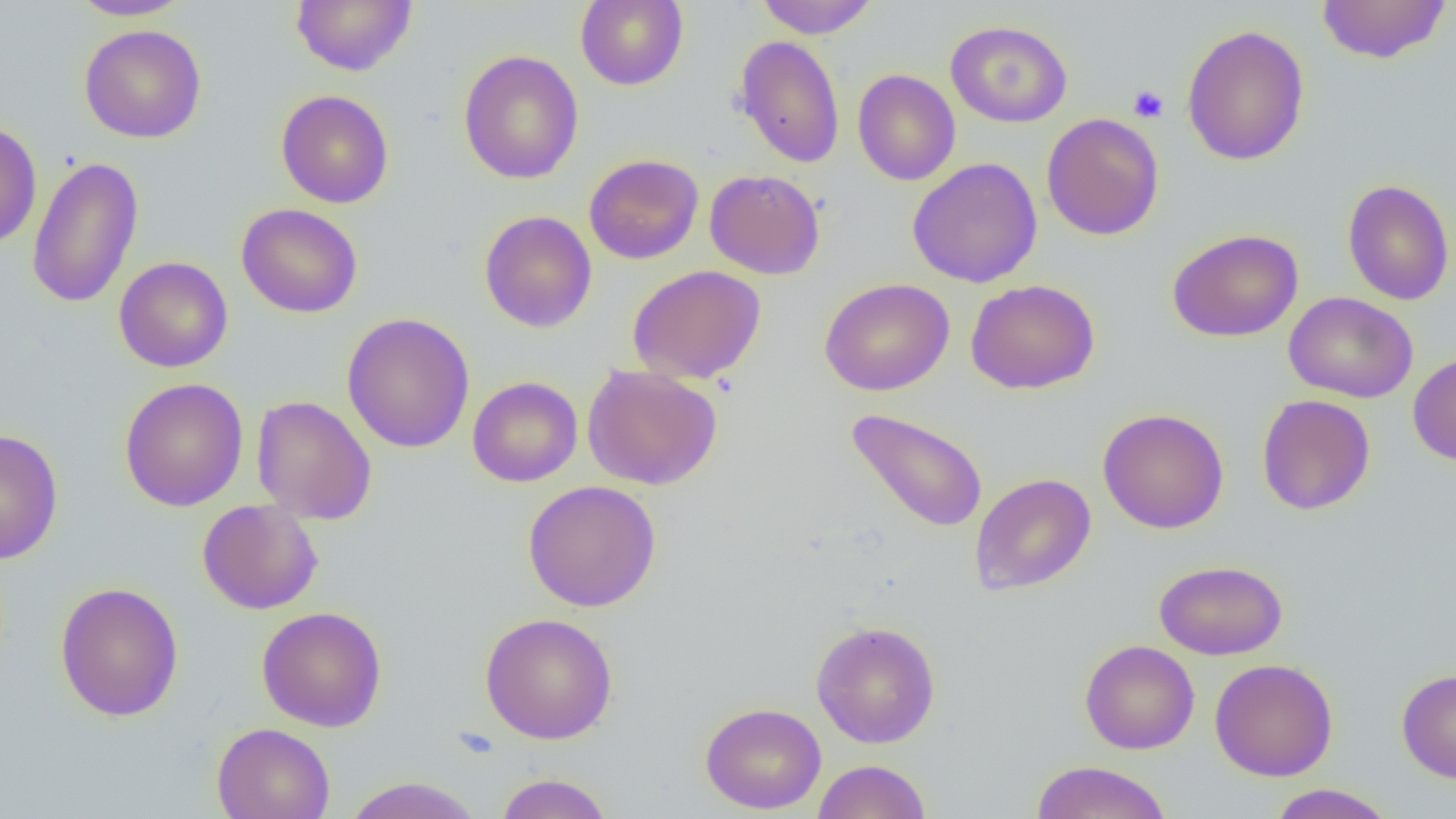

Approximate bounding boxes as named x1/y1/x2/y2 corners in pixels. Uninfected red blood cell locations: (x1=69, y1=0, x2=195, y2=21), (x1=291, y1=0, x2=417, y2=76), (x1=575, y1=0, x2=689, y2=91), (x1=755, y1=0, x2=879, y2=39), (x1=1316, y1=0, x2=1453, y2=64), (x1=945, y1=20, x2=1073, y2=127), (x1=1181, y1=23, x2=1310, y2=166), (x1=79, y1=24, x2=207, y2=143), (x1=734, y1=35, x2=846, y2=169), (x1=458, y1=49, x2=584, y2=184), (x1=852, y1=69, x2=960, y2=186), (x1=276, y1=89, x2=394, y2=209), (x1=1041, y1=113, x2=1165, y2=241), (x1=0, y1=121, x2=42, y2=249), (x1=584, y1=154, x2=704, y2=264), (x1=27, y1=155, x2=144, y2=311), (x1=907, y1=157, x2=1043, y2=288), (x1=704, y1=169, x2=825, y2=280), (x1=1342, y1=179, x2=1455, y2=306), (x1=236, y1=203, x2=363, y2=318), (x1=479, y1=210, x2=597, y2=333), (x1=1167, y1=228, x2=1304, y2=343), (x1=114, y1=256, x2=233, y2=373), (x1=627, y1=265, x2=766, y2=384), (x1=819, y1=277, x2=955, y2=396), (x1=966, y1=279, x2=1100, y2=394), (x1=1284, y1=291, x2=1418, y2=403), (x1=341, y1=312, x2=475, y2=453), (x1=1408, y1=351, x2=1456, y2=466), (x1=582, y1=365, x2=723, y2=490), (x1=467, y1=376, x2=582, y2=487), (x1=119, y1=377, x2=249, y2=512), (x1=251, y1=395, x2=377, y2=524), (x1=1256, y1=395, x2=1376, y2=515), (x1=1098, y1=407, x2=1229, y2=534), (x1=845, y1=408, x2=988, y2=534), (x1=1, y1=428, x2=64, y2=564), (x1=969, y1=473, x2=1096, y2=595), (x1=522, y1=481, x2=662, y2=612), (x1=196, y1=500, x2=323, y2=614), (x1=1154, y1=559, x2=1288, y2=660), (x1=54, y1=581, x2=184, y2=722), (x1=257, y1=606, x2=388, y2=731), (x1=479, y1=612, x2=618, y2=744), (x1=811, y1=620, x2=941, y2=748), (x1=1080, y1=639, x2=1200, y2=754), (x1=1209, y1=658, x2=1339, y2=781), (x1=1396, y1=668, x2=1456, y2=783), (x1=700, y1=702, x2=827, y2=814), (x1=211, y1=723, x2=336, y2=819), (x1=812, y1=759, x2=931, y2=819), (x1=1030, y1=760, x2=1174, y2=819), (x1=495, y1=772, x2=614, y2=819), (x1=341, y1=776, x2=486, y2=819), (x1=1266, y1=784, x2=1397, y2=818). Platelet locations: (x1=1128, y1=84, x2=1168, y2=122). Slide-level diagnosis: negative for blood parasites. Light microscopy. Single field of view. Image is 1456×819 pixels. Captured at 1000x magnification. Thin blood smear.